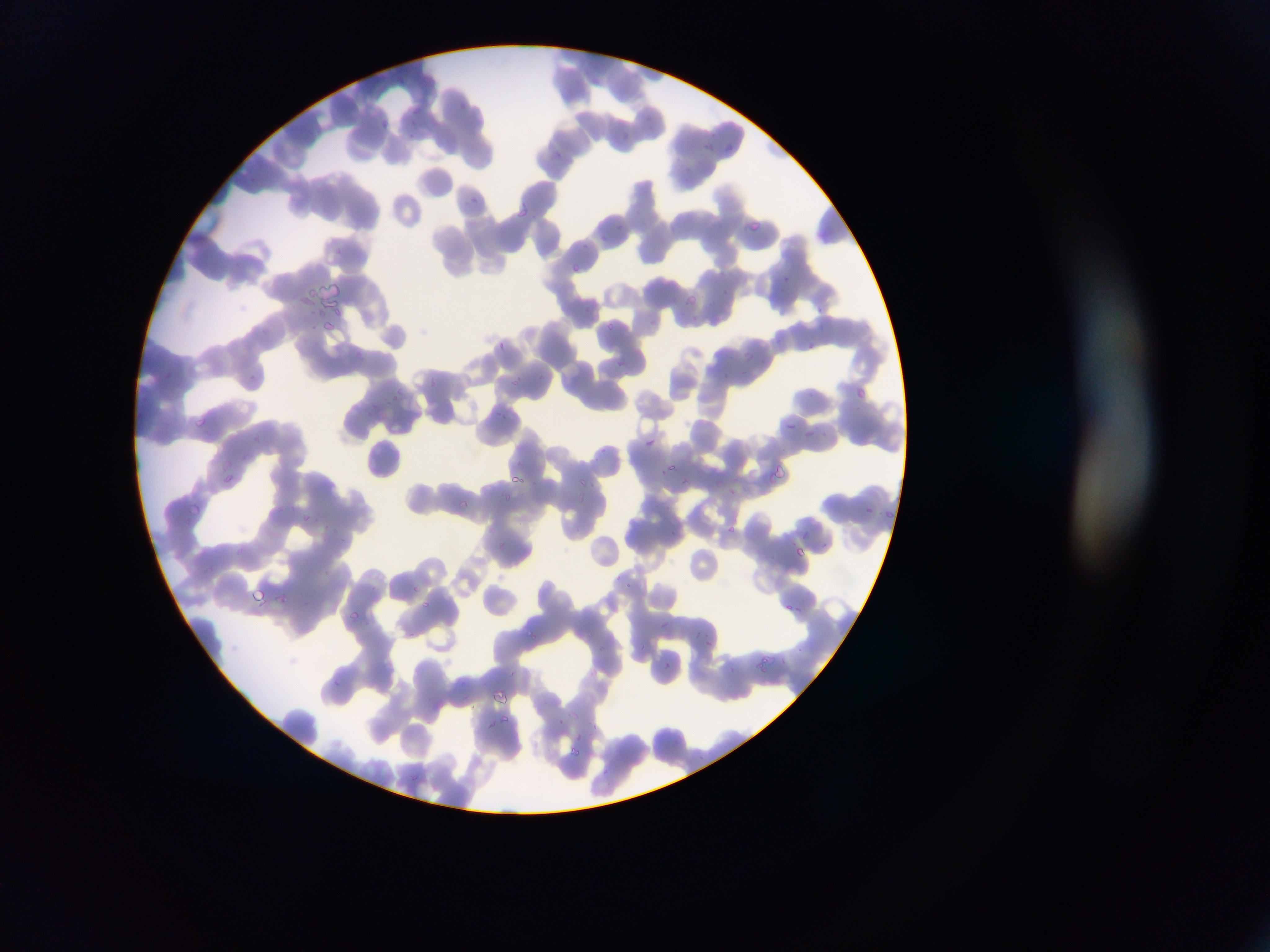

{
  "capture": "mobile-phone photograph through a microscope",
  "plasmodium_parasite_locations": "approximate bounding boxes as {left, top, right, bottom} in pixels: {396, 76, 406, 85}, {459, 101, 462, 109}, {412, 104, 426, 114}, {379, 117, 390, 127}, {620, 131, 639, 141}, {700, 138, 715, 150}, {724, 140, 734, 151}, {552, 147, 563, 158}, {469, 197, 477, 204}, {515, 208, 529, 221}, {748, 219, 767, 229}, {614, 221, 628, 229}, {596, 232, 609, 246}, {568, 263, 580, 274}, {782, 273, 791, 280}, {687, 289, 699, 306}, {813, 300, 825, 319}, {322, 318, 339, 333}, {605, 321, 620, 331}, {775, 334, 786, 344}, {496, 340, 508, 351}, {803, 340, 815, 353}, {742, 351, 753, 365}, {615, 356, 629, 372}, {723, 370, 733, 382}, {248, 371, 257, 385}, {510, 372, 529, 393}, {427, 376, 442, 390}, {858, 386, 867, 400}, {392, 393, 402, 402}, {373, 401, 383, 411}, {194, 418, 208, 431}, {784, 424, 799, 432}, {804, 427, 817, 439}, {642, 436, 659, 446}, {598, 445, 612, 462}, {667, 464, 679, 469}, {778, 464, 793, 476}, {766, 472, 778, 485}, {509, 473, 523, 486}, {218, 474, 232, 482}, {673, 476, 690, 490}, {579, 478, 586, 490}, {729, 485, 741, 501}, {501, 493, 515, 503}, {457, 497, 471, 511}, {188, 500, 202, 514}, {865, 504, 880, 515}, {885, 507, 897, 517}, {304, 509, 315, 525}, {728, 525, 739, 534}, {801, 531, 810, 542}, {797, 545, 805, 557}, {626, 579, 637, 596}, {412, 583, 424, 593}, {252, 584, 264, 603}, {272, 589, 286, 604}, {423, 599, 429, 607}, {785, 600, 803, 619}, {348, 609, 360, 623}, {655, 620, 669, 633}, {529, 625, 541, 639}, {693, 628, 699, 637}, {705, 637, 711, 647}, {754, 658, 773, 676}, {664, 660, 672, 669}, {726, 663, 736, 673}, {328, 678, 343, 691}, {493, 689, 512, 701}, {501, 713, 512, 725}, {559, 716, 567, 726}, {488, 718, 495, 731}, {591, 721, 602, 731}, {571, 744, 585, 755}, {600, 767, 614, 779} | approximate {x, y} pixel centers of objects too small to bound: {337, 250}, {618, 576}, {580, 735}",
  "preparation": "thin blood smear",
  "field_of_view": "single",
  "country": "Ghana",
  "image_size": "1270×952 pixels"
}